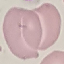

Summary:
  - Malaria status: uninfected
  - Stain: Giemsa
  - Preparation: thin blood film
  - Image type: cell patch, automatically extracted from a larger field of view and resized to 64 × 64 pixels
  - Capture: smartphone camera at the microscope eyepiece